Comment on the morphology of the erythrocytes.
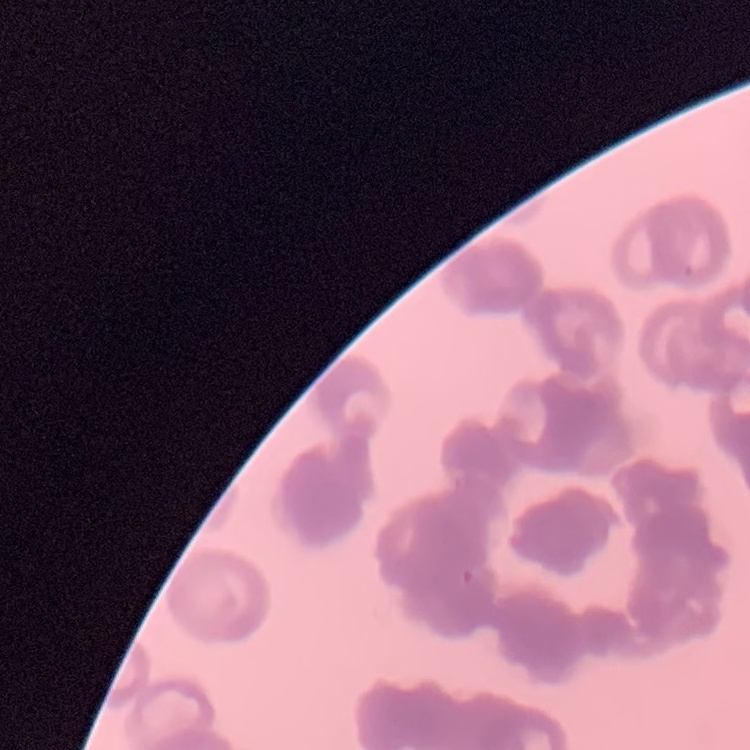

Rouleaux formation.

stain = Field's or Giemsa
image type = one tile cut from a larger photomicrograph
preparation = thin blood film